Outline each Plasmodium ovale-infected red blood cell.
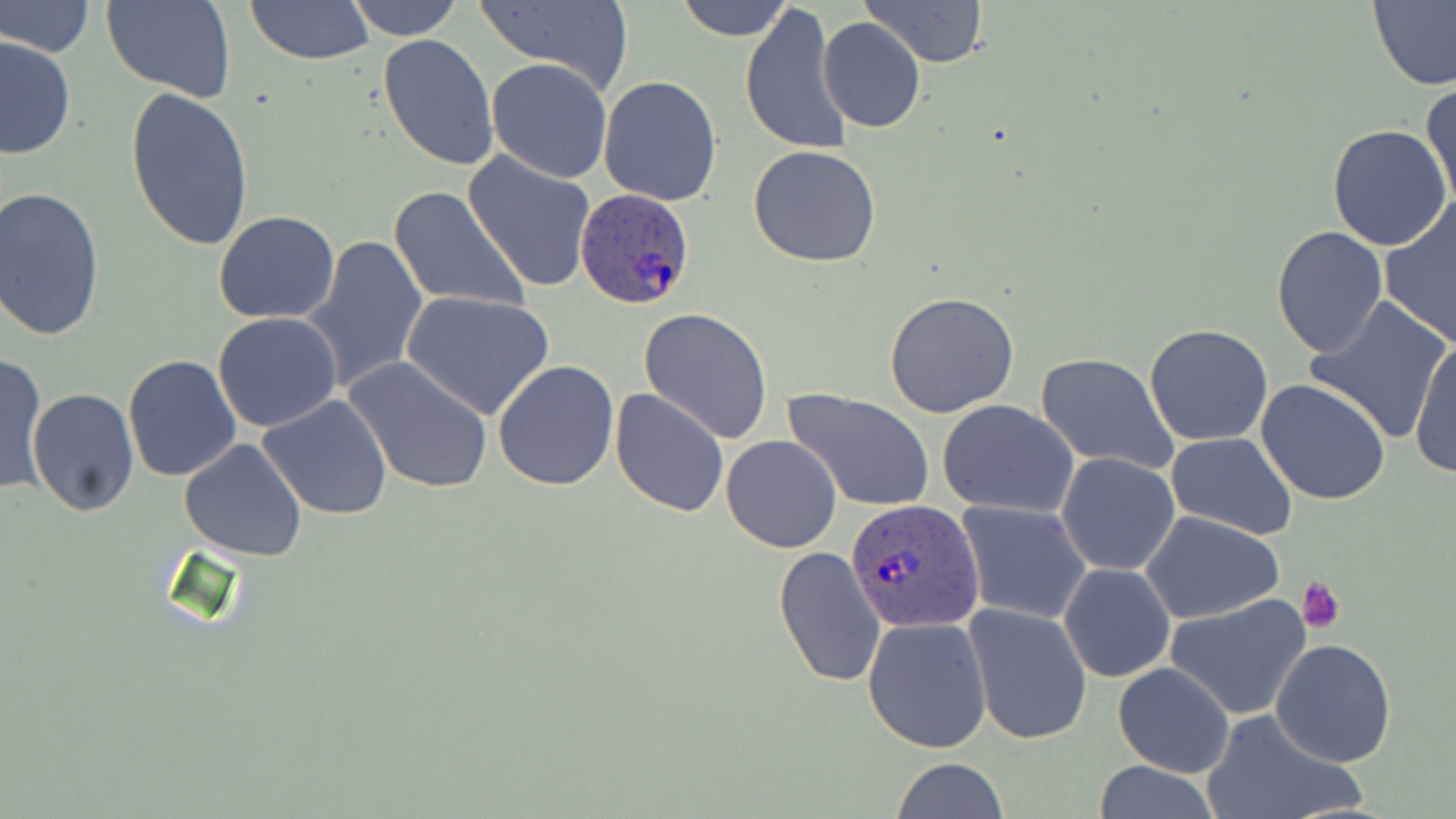

Approximate bounding boxes as named x1/y1/x2/y2 corners in pixels.
Plasmodium ovale-infected red blood cells: (x1=575, y1=187, x2=698, y2=312), (x1=848, y1=500, x2=982, y2=634).

slide_level_diagnosis: Plasmodium ovale
stain: May-Grünwald-Giemsa
platelet_locations: 'approximate bounding boxes as named x1/y1/x2/y2 corners in pixels: (x1=1298, y1=576, x2=1346, y2=634)'
magnification: 1000x
preparation: thin blood smear
field_of_view: one of a larger specimen
image_size: 1456×819 pixels
modality: light microscopy
uninfected_red_blood_cell_locations: 'approximate bounding boxes as named x1/y1/x2/y2 corners in pixels: (x1=102, y1=0, x2=237, y2=101), (x1=246, y1=0, x2=373, y2=65), (x1=347, y1=0, x2=463, y2=40), (x1=860, y1=0, x2=987, y2=68), (x1=1369, y1=0, x2=1456, y2=92), (x1=1, y1=1, x2=96, y2=58), (x1=475, y1=1, x2=633, y2=95), (x1=676, y1=1, x2=793, y2=42), (x1=739, y1=4, x2=851, y2=154), (x1=817, y1=17, x2=926, y2=134), (x1=377, y1=33, x2=499, y2=171), (x1=1, y1=35, x2=76, y2=161), (x1=485, y1=58, x2=614, y2=184), (x1=599, y1=76, x2=721, y2=207), (x1=1421, y1=81, x2=1455, y2=214), (x1=125, y1=85, x2=255, y2=251), (x1=1327, y1=124, x2=1454, y2=250), (x1=749, y1=145, x2=881, y2=267), (x1=463, y1=152, x2=598, y2=292), (x1=389, y1=185, x2=530, y2=314), (x1=0, y1=188, x2=105, y2=341), (x1=1378, y1=200, x2=1456, y2=348), (x1=213, y1=211, x2=340, y2=324), (x1=1272, y1=225, x2=1389, y2=359), (x1=300, y1=232, x2=429, y2=398), (x1=884, y1=291, x2=1020, y2=417), (x1=402, y1=292, x2=556, y2=420), (x1=1302, y1=297, x2=1452, y2=442), (x1=639, y1=308, x2=772, y2=443), (x1=212, y1=312, x2=343, y2=433), (x1=1144, y1=324, x2=1274, y2=446), (x1=1409, y1=334, x2=1456, y2=479), (x1=1, y1=352, x2=47, y2=495), (x1=1036, y1=352, x2=1179, y2=474), (x1=122, y1=353, x2=241, y2=482), (x1=345, y1=357, x2=492, y2=495), (x1=493, y1=359, x2=619, y2=489), (x1=1256, y1=377, x2=1390, y2=506), (x1=609, y1=387, x2=729, y2=518), (x1=27, y1=388, x2=138, y2=516), (x1=784, y1=389, x2=935, y2=512), (x1=257, y1=395, x2=393, y2=520), (x1=937, y1=400, x2=1078, y2=519), (x1=1166, y1=433, x2=1297, y2=539), (x1=721, y1=435, x2=844, y2=553), (x1=178, y1=438, x2=308, y2=561), (x1=1056, y1=453, x2=1181, y2=576), (x1=957, y1=500, x2=1094, y2=624), (x1=1140, y1=512, x2=1284, y2=625), (x1=773, y1=546, x2=887, y2=688), (x1=1059, y1=561, x2=1176, y2=682), (x1=1166, y1=592, x2=1312, y2=720), (x1=964, y1=603, x2=1092, y2=744), (x1=862, y1=618, x2=992, y2=752), (x1=1270, y1=638, x2=1397, y2=768), (x1=1112, y1=662, x2=1235, y2=779), (x1=1204, y1=708, x2=1365, y2=819), (x1=889, y1=759, x2=1010, y2=819), (x1=1088, y1=760, x2=1225, y2=818)'